Identify the preparation type.
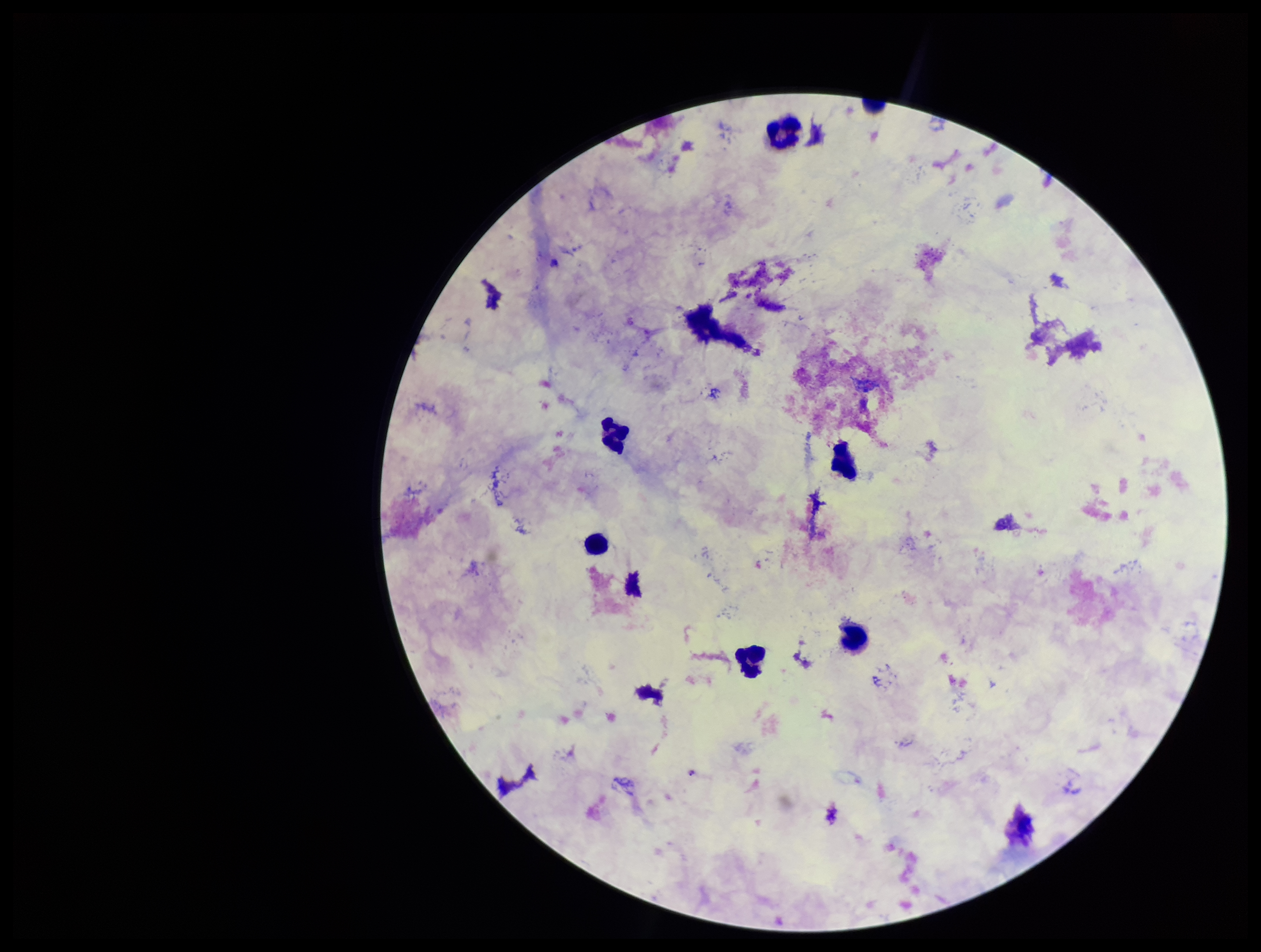
It is a thick blood smear.

capture = smartphone photograph through the microscope eyepiece
leukocyte count = 6
field of view = single
image size = 1261×952 pixels
patient malaria status = negative
parasite count = 0
stain = Giemsa
Plasmodium parasites = none seen